Point out each Plasmodium parasite.
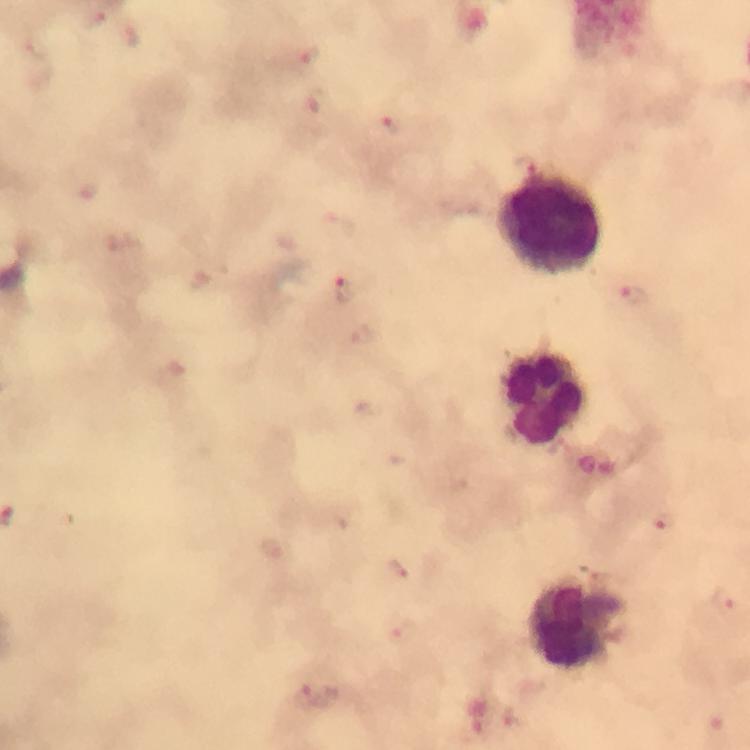

Approximate centers as {x, y} in pixels.
Plasmodium parasites: {96, 19}, {131, 37}, {309, 56}, {319, 100}, {392, 124}, {525, 164}, {344, 287}, {632, 295}, {664, 519}, {400, 569}, {725, 601}, {403, 630}, {319, 696}.

Summary:
  - Leukocyte locations: {549, 224}, {543, 396}, {576, 623}
  - Magnification: 100x
  - Image size: 750×750 pixels
  - Capture: smartphone camera through the microscope
  - Preparation: thick smear
  - Immersion oil: used
  - Context: from a diagnostic examination for malaria
  - Cropped from: one field of view
  - Stain: Giemsa